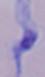
Summary:
  - Identification: trypanosome
  - Modality: micrograph
  - Magnification: 1000x